Outline each blood parasite and name the species.
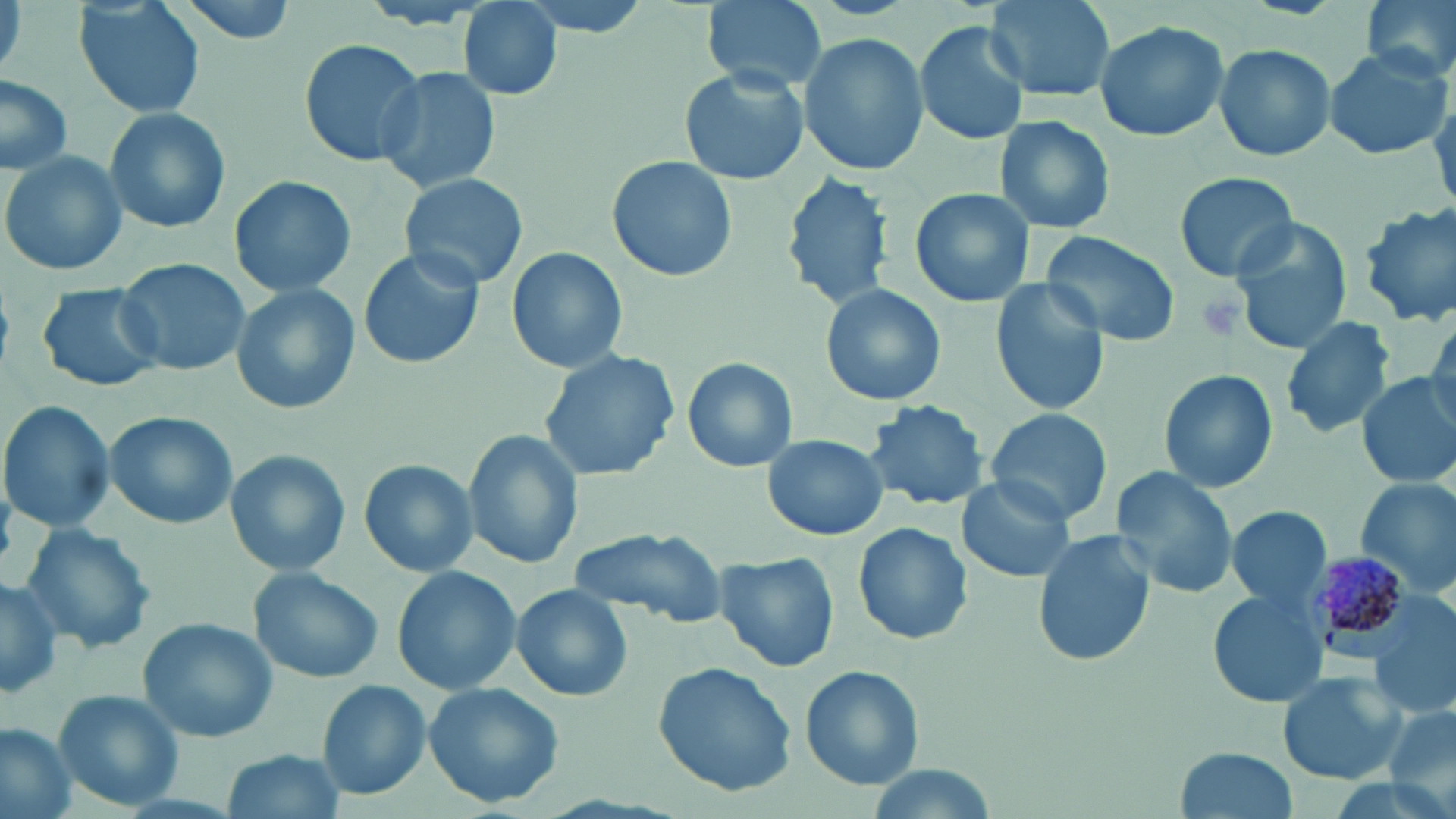
Approximate bounding boxes as [x1, y1, x2, y2] in pixels.
Plasmodium malariae-infected red blood cells: [1306, 557, 1419, 665].
No Plasmodium falciparum, Plasmodium ovale, Plasmodium vivax, Babesia divergens, or Trypanosoma brucei observed.

slide-level diagnosis = Plasmodium malariae
field of view = single
modality = light microscopy
preparation = thin blood smear
magnification = 1000x
platelet locations = approximate bounding boxes as [x1, y1, x2, y2] in pixels: [1195, 290, 1248, 342]
stain = May-Grünwald-Giemsa
image size = 1456×819 pixels
uninfected red blood cell locations = approximate bounding boxes as [x1, y1, x2, y2] in pixels: [75, 0, 205, 120], [162, 0, 305, 44], [510, 0, 655, 36], [699, 0, 828, 91], [984, 0, 1115, 104], [1358, 0, 1456, 79], [0, 1, 26, 80], [458, 2, 565, 102], [1091, 19, 1230, 142], [915, 21, 1029, 144], [800, 33, 927, 176], [297, 37, 428, 167], [1214, 42, 1336, 163], [1322, 46, 1452, 159], [372, 66, 501, 196], [678, 66, 810, 185], [0, 77, 72, 172], [103, 105, 231, 235], [991, 116, 1118, 236], [0, 150, 127, 276], [606, 156, 736, 284], [1170, 170, 1301, 283], [781, 171, 896, 311], [399, 172, 529, 291], [228, 174, 358, 299], [909, 188, 1031, 309], [1354, 201, 1456, 328], [1230, 218, 1352, 354], [1039, 228, 1179, 347], [357, 247, 484, 372], [508, 248, 626, 372], [114, 257, 253, 378], [989, 278, 1109, 415], [229, 283, 361, 416], [818, 283, 948, 408], [36, 284, 164, 392], [1424, 312, 1456, 431], [1280, 316, 1396, 439], [538, 348, 681, 484], [682, 358, 797, 472], [1158, 369, 1278, 493], [1355, 372, 1455, 490], [863, 398, 991, 511], [0, 399, 116, 534], [985, 406, 1112, 525], [104, 411, 236, 531], [463, 428, 585, 569], [763, 434, 887, 541], [223, 449, 352, 577], [360, 460, 477, 578], [1110, 467, 1240, 598], [956, 476, 1076, 583], [1355, 477, 1456, 598], [1224, 505, 1333, 609], [18, 523, 157, 655], [853, 523, 973, 646], [567, 528, 727, 626], [1031, 528, 1155, 667], [713, 550, 839, 675], [391, 565, 520, 696], [247, 568, 384, 684], [0, 573, 63, 697], [511, 584, 630, 702], [1207, 588, 1327, 709], [1372, 615, 1455, 725], [139, 616, 282, 742], [652, 662, 797, 796], [800, 665, 922, 789], [1276, 670, 1409, 785], [318, 681, 432, 800], [422, 682, 566, 810], [52, 687, 186, 812], [1378, 704, 1456, 807], [1, 726, 76, 818], [1173, 746, 1302, 819], [220, 749, 345, 819]